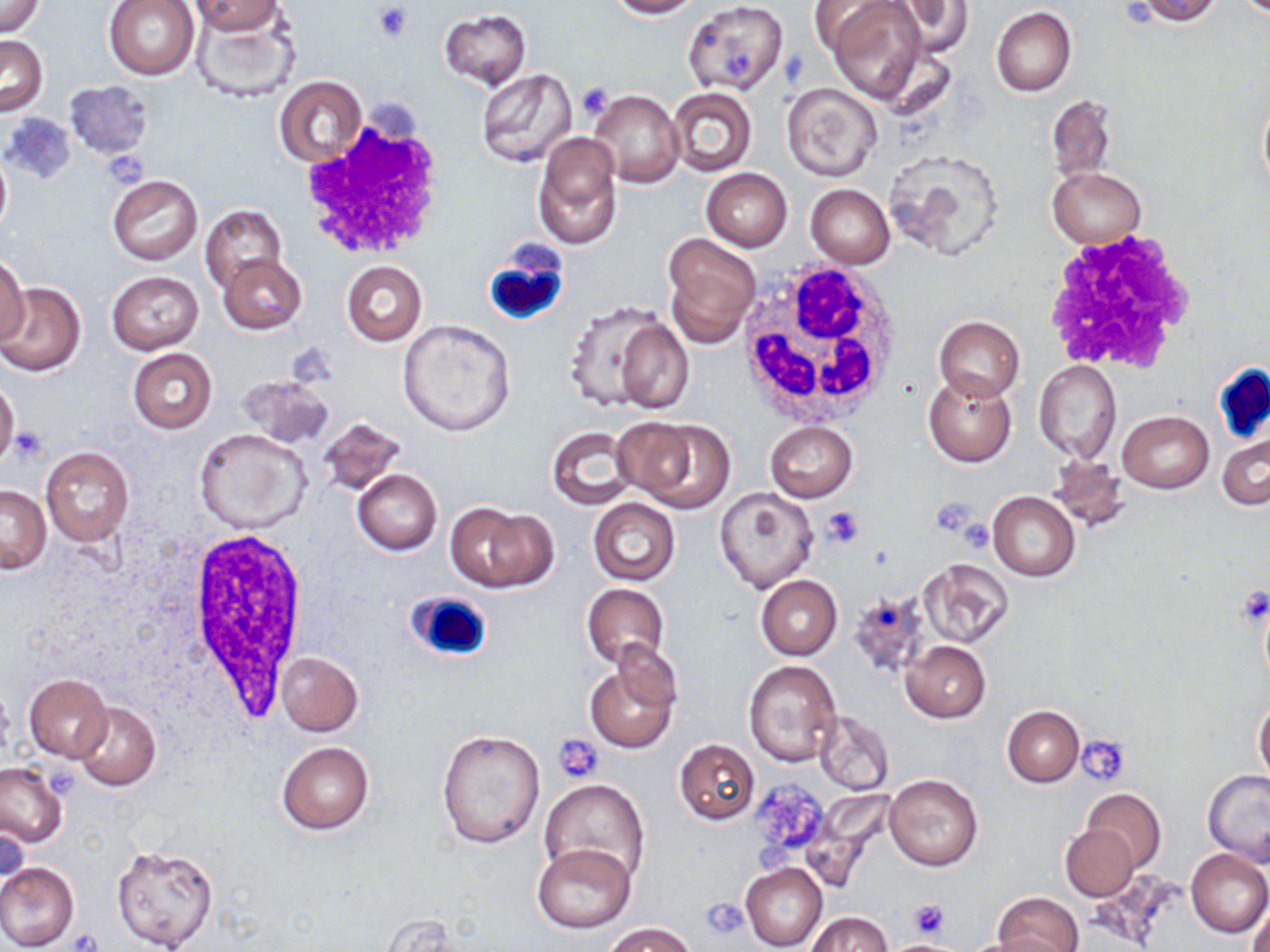
slide-level diagnosis = negative for blood parasites
field of view = one of a larger specimen
stain = May-Grünwald-Giemsa
preparation = thin blood film
modality = light microscopy
white blood cell locations = approximate bounding boxes as (x1,y1)-(x2,y2) corner pairs in pixels: (302,117)-(447,259), (1037,230)-(1200,374), (482,246)-(569,326), (738,258)-(906,426), (1213,362)-(1270,446), (182,527)-(305,716), (405,589)-(495,665)
magnification = 1000x
uninfected red blood cell locations = approximate bounding boxes as (x1,y1)-(x2,y2) corner pairs in pixels: (1,0)-(45,37), (103,0)-(200,80), (190,0)-(284,36), (604,0)-(704,19), (682,0)-(789,96), (886,0)-(972,59), (1132,0)-(1221,26), (806,1)-(898,54), (827,1)-(929,102), (193,4)-(301,104), (992,6)-(1076,96), (438,9)-(532,89), (0,35)-(48,115), (476,70)-(579,172), (274,76)-(368,167), (63,80)-(155,160), (781,82)-(883,182), (666,87)-(757,177), (590,90)-(684,188), (1045,94)-(1118,182), (1256,94)-(1270,194), (533,133)-(623,251), (0,145)-(11,238), (885,148)-(1005,259), (1048,168)-(1146,248), (701,169)-(792,251), (107,175)-(202,265), (806,184)-(896,269), (199,204)-(288,292), (663,232)-(760,345), (219,252)-(307,333), (0,257)-(29,346), (341,261)-(427,346), (106,271)-(203,355), (0,282)-(86,377), (563,300)-(689,415), (933,315)-(1025,401), (398,318)-(515,436), (127,349)-(218,435), (1033,361)-(1122,465), (923,372)-(1018,468), (238,373)-(337,451), (0,374)-(19,470), (1118,409)-(1214,493), (621,416)-(735,512), (317,417)-(407,498), (764,421)-(857,502), (547,426)-(638,510), (194,429)-(312,533), (1216,432)-(1269,512), (40,447)-(134,546), (1048,451)-(1130,531), (352,469)-(442,554), (0,485)-(51,575), (714,489)-(818,593), (989,491)-(1080,581), (589,499)-(680,586), (446,502)-(556,593), (918,559)-(1014,647), (755,575)-(843,661), (580,583)-(669,670), (850,588)-(932,680), (900,641)-(991,723), (276,652)-(363,737), (585,658)-(679,753), (743,660)-(841,766), (23,674)-(111,762), (1254,698)-(1270,786), (71,701)-(160,792), (1002,705)-(1084,787), (812,710)-(894,797), (435,727)-(545,850), (674,739)-(760,824), (276,741)-(374,835), (0,762)-(68,849), (1203,770)-(1270,867), (884,774)-(983,871), (538,780)-(651,886), (1082,788)-(1166,871), (1,819)-(29,900), (1059,824)-(1139,901), (111,843)-(221,952), (532,843)-(635,933), (1185,848)-(1270,937), (0,861)-(79,952), (740,862)-(827,952), (993,892)-(1085,952), (1247,894)-(1269,952), (806,912)-(894,952), (606,922)-(696,952), (954,935)-(1056,952)
image size = 1270×952 pixels
platelet locations = approximate bounding boxes as (x1,y1)-(x2,y2) corner pairs in pixels: (372,4)-(413,41), (724,52)-(754,79), (577,82)-(615,120), (104,150)-(149,185), (9,427)-(49,465), (931,496)-(982,536), (821,506)-(865,548), (955,519)-(995,555), (1233,583)-(1270,629), (553,734)-(604,783), (1078,735)-(1132,785), (750,781)-(832,848), (755,839)-(795,881), (702,895)-(751,941), (908,899)-(950,939), (69,927)-(104,952), (889,941)-(959,952)